Report the malaria status of this cell.
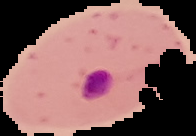

Parasitized.

{
  "preparation": "thin blood smear",
  "image_type": "segmented cell region on a black background",
  "image_size": "196×136 pixels"
}